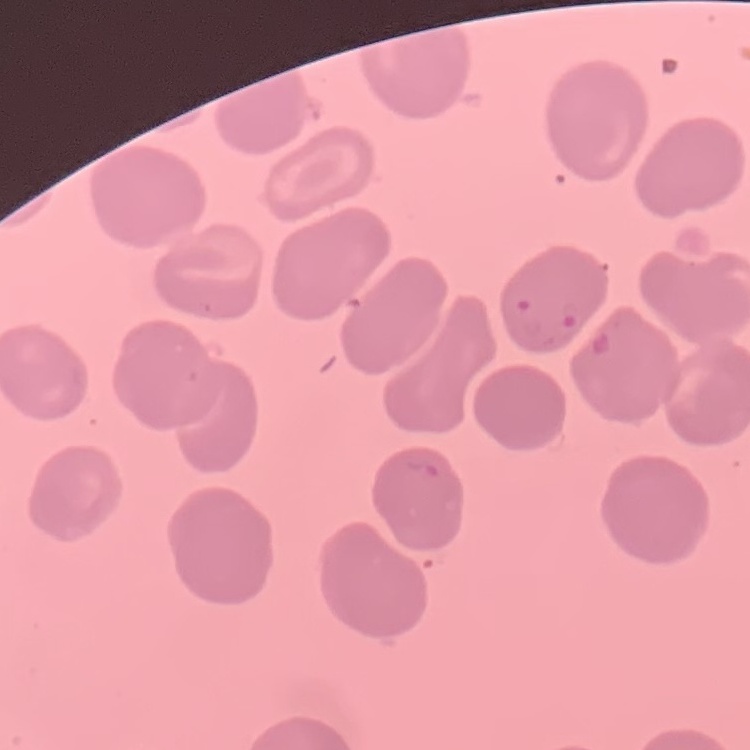
Summary:
  - Erythrocyte morphology: no rouleaux formation
  - Image type: square crop of a larger photomicrograph
  - Preparation: thin blood film
  - Stain: Field's or Giemsa